State which parasite is depicted.
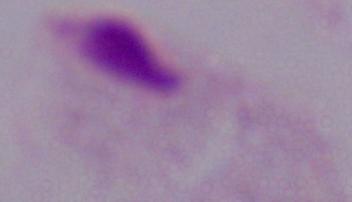

A trichomonad.

modality = micrograph
magnification = 1000x